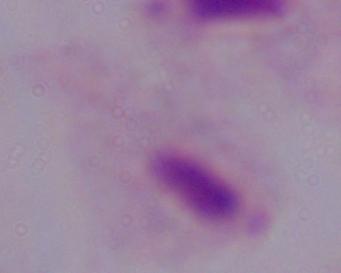

modality: photomicrograph
identification: trichomonad
magnification: 1000x